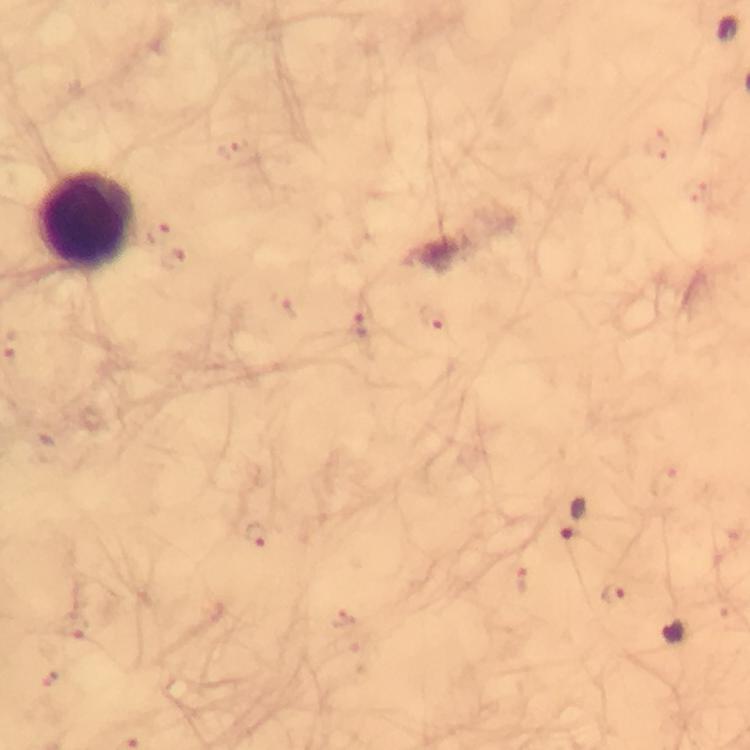
Approximate centers as [x, y] in pixels. Malaria parasite locations: [236, 151], [157, 232], [174, 258], [433, 323], [362, 325], [573, 517], [257, 535], [523, 582], [614, 594], [340, 618], [74, 627], [51, 680]. Leukocyte locations: [87, 220]. A crop from one field of view. Image is 750×750 pixels. 100x magnification. From a malaria diagnostic workup. Immersion oil was used. Giemsa-stained preparation. Thick smear. Photographed with a smartphone mounted on the microscope.